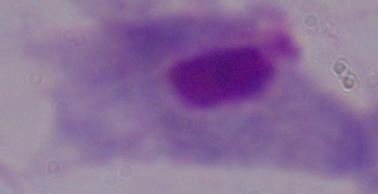

Summary:
  - Modality: photomicrograph
  - Identification: trichomonad
  - Magnification: 1000x